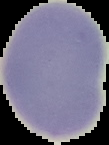
Summary:
  - Result: no Plasmodium parasites detected
  - Image type: cell region segmented out of the field of view; surrounding area masked to black
  - Preparation: thin blood film
  - Image size: 109×145 pixels